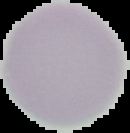

{
  "preparation": "thin blood smear",
  "result": "negative for malaria parasites",
  "image_type": "segmented cell region with the area outside set to black",
  "image_size": "130×133 pixels"
}